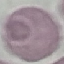

Summary:
  - Result: no malaria parasites detected
  - Preparation: thin blood film
  - Image type: automatically extracted cell patch, resized to 64 × 64 pixels
  - Stain: Giemsa
  - Capture: smartphone through the microscope eyepiece